Identify the cell.
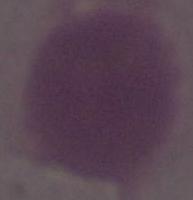

An erythrocyte.

Captured at 1000x magnification. Micrograph.